Locate every malaria parasite and every leukocyte.
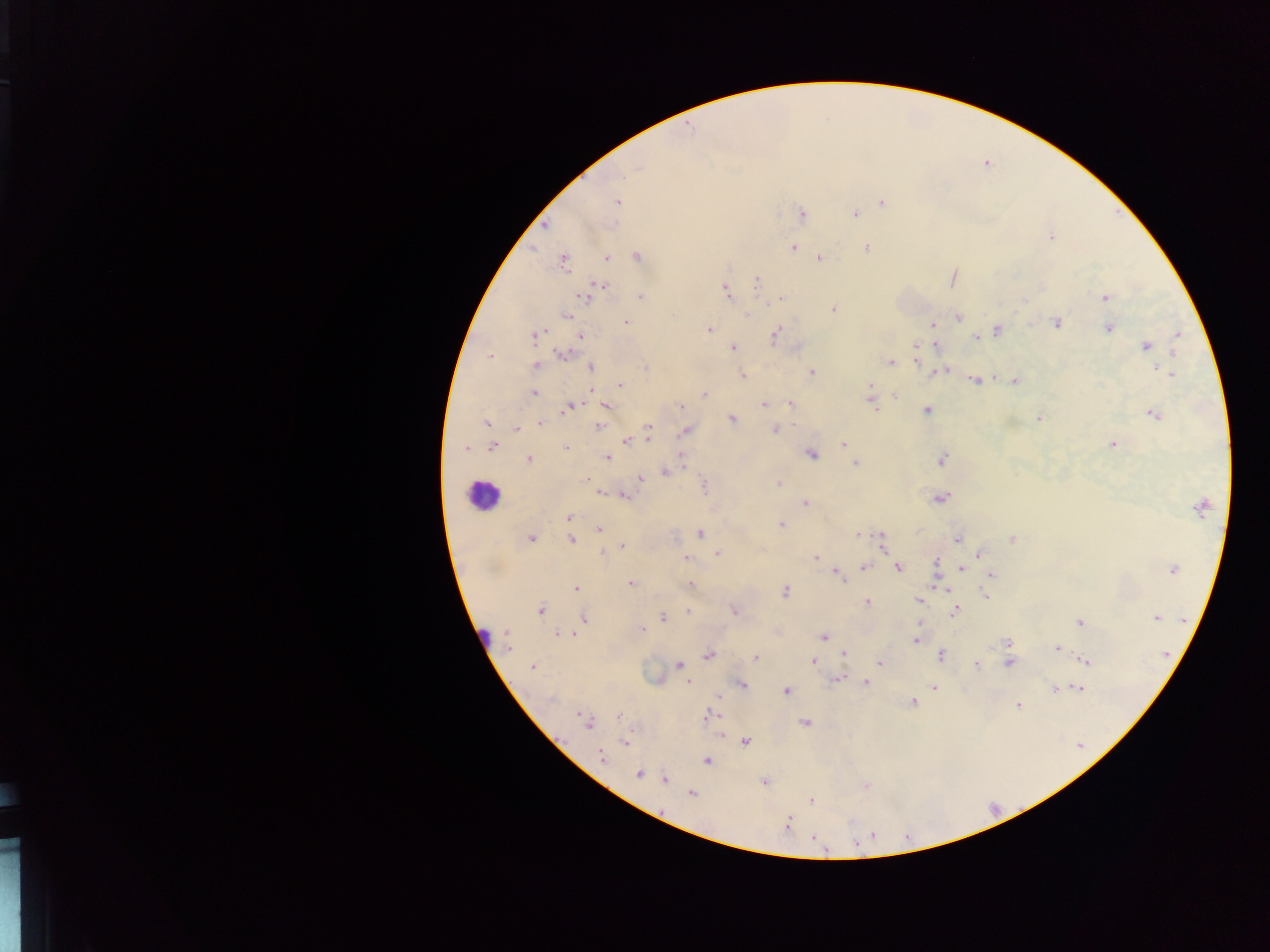
Approximate centers as x y in pixels.
Malaria parasites: 637 168; 617 202; 882 202; 802 213; 856 214; 544 226; 1052 237; 793 247; 867 248; 607 257; 638 257; 819 258; 563 262; 756 281; 597 288; 726 292; 588 295; 640 296; 1105 298; 781 299; 833 309; 747 315; 567 316; 958 317; 626 322; 1056 323; 933 324; 1108 328; 709 329; 998 330; 535 334; 1179 334; 775 335; 582 336; 976 337; 935 344; 916 346; 1147 346; 733 347; 563 353; 491 356; 916 361; 890 363; 536 365; 591 368; 644 368; 941 371; 812 372; 1169 374; 743 375; 975 381; 1014 382; 620 386; 870 386; 533 393; 869 394; 705 395; 896 396; 764 404; 790 404; 605 405; 681 406; 872 406; 570 408; 926 411; 1154 414; 1038 418; 731 419; 486 423; 540 423; 599 426; 517 428; 649 428; 775 430; 685 431; 649 435; 626 441; 843 444; 1112 445; 492 447; 566 447; 465 449; 811 453; 682 456; 607 458; 529 459; 941 460; 855 463; 665 471; 640 478; 587 479; 779 483; 705 485; 600 492; 624 496; 940 498; 805 504; 1199 508; 569 517; 780 524; 598 529; 700 534; 859 535; 531 538; 881 539; 958 539; 572 540; 1012 540; 623 546; 882 546; 602 554; 718 554; 980 555; 816 557; 685 558; 935 563; 864 567; 961 567; 898 568; 1173 569; 991 575; 840 576; 631 584; 690 585; 942 586; 575 588; 784 591; 985 595; 919 601; 867 603; 540 611; 688 611; 734 611; 955 612; 663 618; 1155 618; 585 619; 1081 621; 642 629; 506 633; 564 634; 824 636; 508 640; 916 640; 1008 642; 1057 648; 843 653; 1166 654; 708 656; 940 656; 755 657; 1087 660; 811 661; 879 662; 1009 662; 679 664; 976 665; 532 666; 838 680; 688 682; 865 683; 741 685; 934 687; 1081 689; 786 690; 1056 690; 718 698; 550 699; 914 702; 1018 706; 708 715; 580 716; 619 716; 588 723; 805 723; 745 742; 624 743; 601 756; 707 761; 638 774; 664 780; 764 782; 692 794; 811 800; 787 824; 873 836; 815 839; 855 843; 825 852.
Leukocytes: 483 495; 483 634.

Sample from Ghana. One field of view. Image is 1270×952 pixels. Thick blood smear. Photographed through a microscope with a mobile-phone camera.